Describe the morphology of the red blood cells.
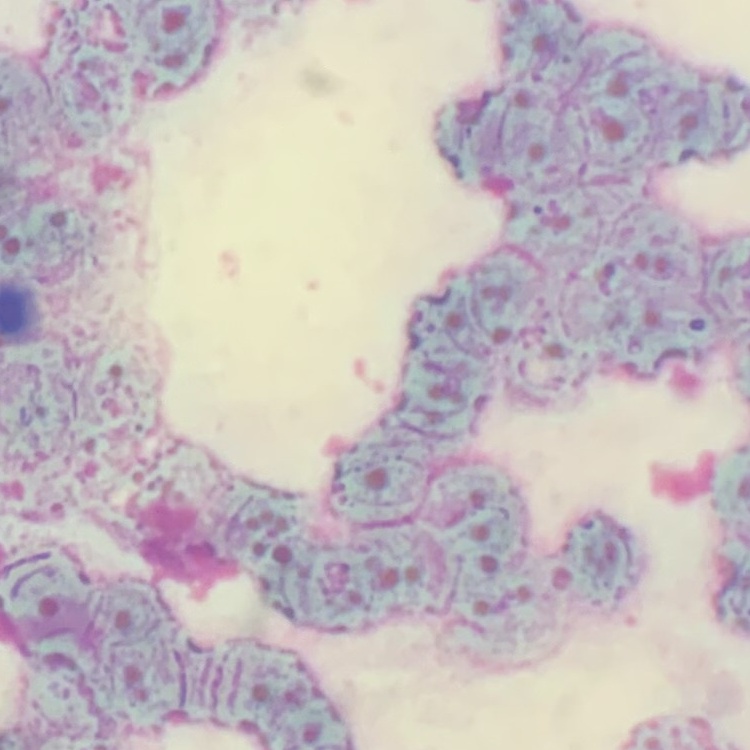

They show rouleaux formation.

preparation = thin blood film
image type = square crop of a larger photomicrograph
stain = Field's or Giemsa